Describe the morphology of the erythrocytes.
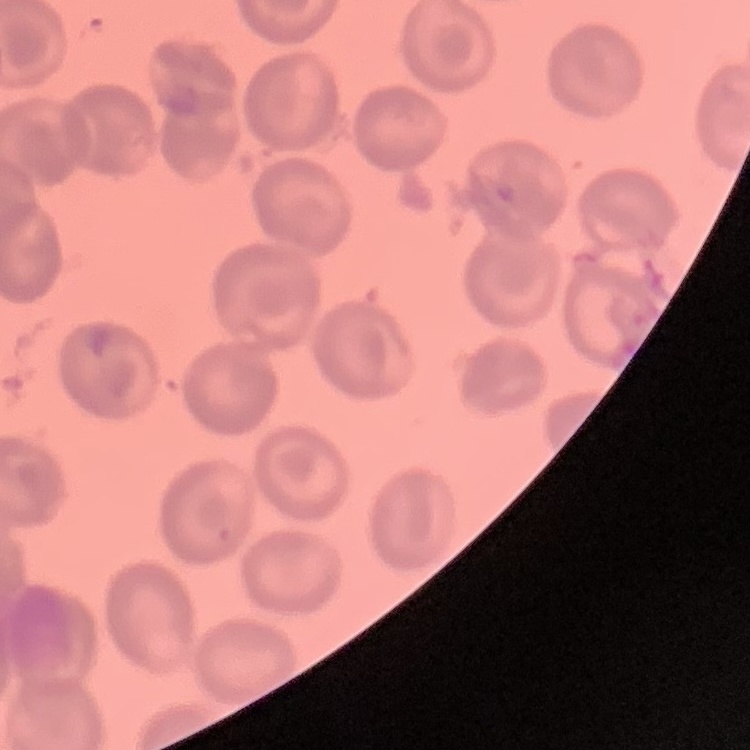

No rouleaux formation.

Summary:
  - Preparation: thin blood film
  - Stain: Field's or Giemsa
  - Image type: one tile cut from a larger photomicrograph